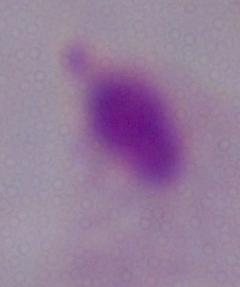

{
  "identification": "trichomonad",
  "magnification": "1000x",
  "modality": "micrograph"
}